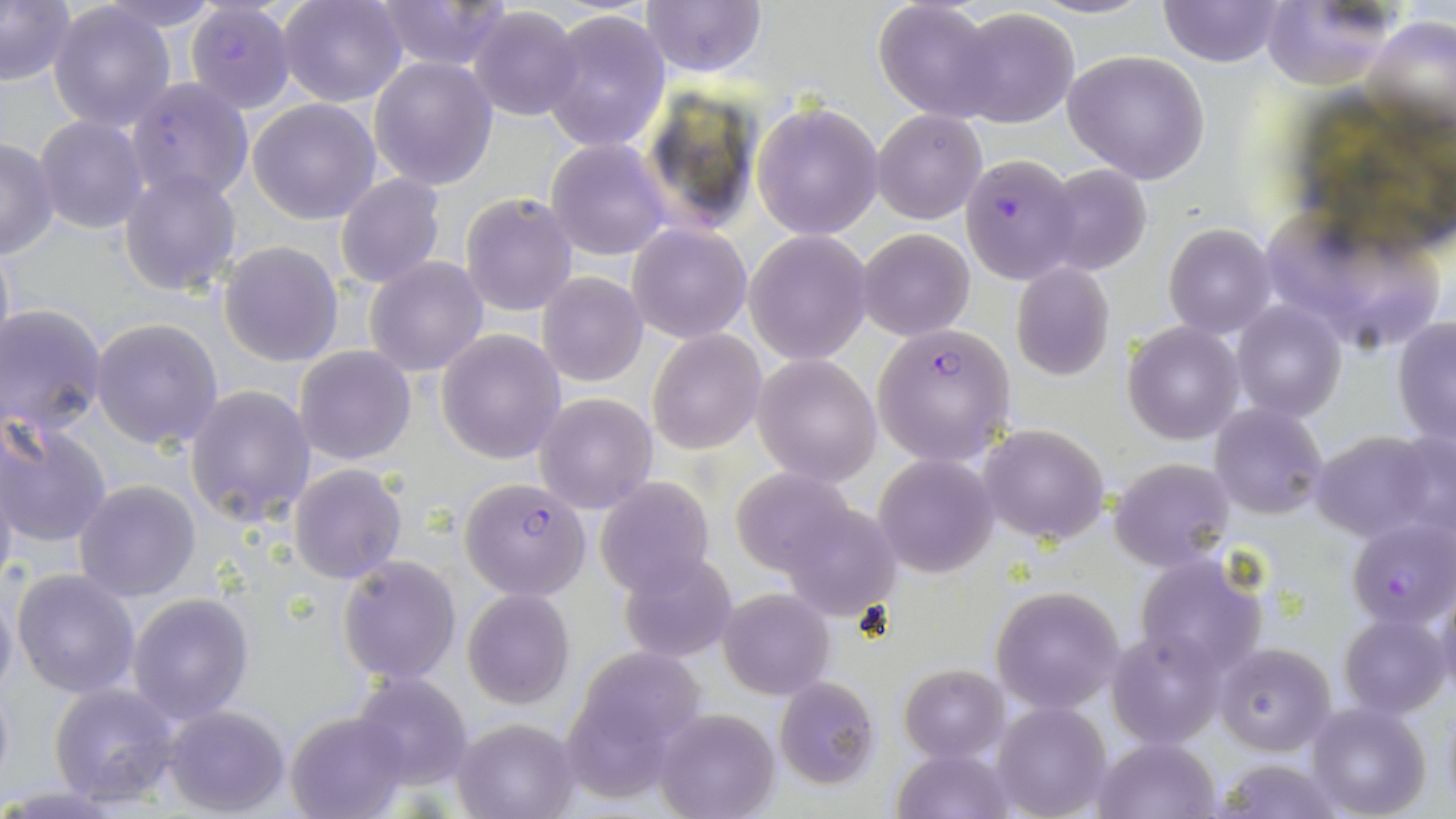

Approximate bounding boxes as (x1,y1)-(x2,y2) corner pairs in pixels. Plasmodium falciparum-infected red blood cell locations: (184,3)-(294,113), (125,77)-(255,203), (959,153)-(1080,284), (872,323)-(1017,467), (458,475)-(592,601), (1347,518)-(1455,630). Uninfected red blood cell locations: (0,0)-(77,89), (93,0)-(225,33), (279,0)-(407,107), (371,0)-(514,71), (640,0)-(767,77), (1020,0)-(1157,20), (1154,0)-(1289,68), (47,1)-(178,133), (876,1)-(1001,120), (1259,1)-(1402,91), (468,6)-(584,122), (542,9)-(672,153), (948,9)-(1079,127), (1364,12)-(1456,144), (1063,49)-(1211,184), (368,56)-(498,190), (247,97)-(383,224), (753,102)-(883,239), (873,109)-(987,224), (33,115)-(149,234), (0,138)-(58,259), (547,139)-(670,260), (1041,165)-(1151,276), (116,168)-(241,298), (335,173)-(445,289), (460,193)-(578,316), (1263,205)-(1381,308), (628,222)-(752,344), (1163,222)-(1277,339), (858,228)-(975,341), (1326,229)-(1447,351), (0,230)-(16,372), (745,231)-(873,364), (219,240)-(344,369), (365,256)-(490,376), (1010,262)-(1115,382), (538,272)-(648,386), (1231,301)-(1346,423), (2,306)-(108,435), (1392,317)-(1456,447), (91,318)-(223,449), (1123,321)-(1244,444), (647,329)-(766,454), (437,330)-(567,464), (295,346)-(417,465), (754,353)-(882,485), (184,384)-(316,527), (534,391)-(658,513), (1210,402)-(1328,519), (1,416)-(112,550), (979,423)-(1110,545), (1308,429)-(1448,542), (876,454)-(999,577), (0,457)-(19,598), (1110,458)-(1234,570), (290,462)-(409,583), (730,470)-(860,577), (595,477)-(715,597), (74,480)-(202,602), (776,502)-(901,622), (617,551)-(739,664), (1133,552)-(1269,682), (337,554)-(462,684), (11,567)-(141,699), (0,579)-(19,707), (993,584)-(1127,713), (1432,584)-(1456,703), (718,587)-(834,699), (462,588)-(575,710), (128,593)-(254,722), (1339,612)-(1449,718), (1108,627)-(1225,749), (1216,644)-(1335,753), (573,650)-(705,780), (899,664)-(1009,761), (351,670)-(473,788), (773,676)-(880,789), (49,683)-(183,807), (991,702)-(1111,819), (1308,702)-(1431,819), (163,704)-(290,816), (654,708)-(779,819), (285,711)-(408,819), (453,716)-(579,819), (1094,738)-(1218,818), (894,748)-(1014,819), (1212,758)-(1347,818). Slide-level diagnosis: Plasmodium falciparum. May-Grünwald-Giemsa stain. Image is 1456×819 pixels. Captured at 1000x magnification. One field of a larger specimen. Light microscopy. Thin blood smear.